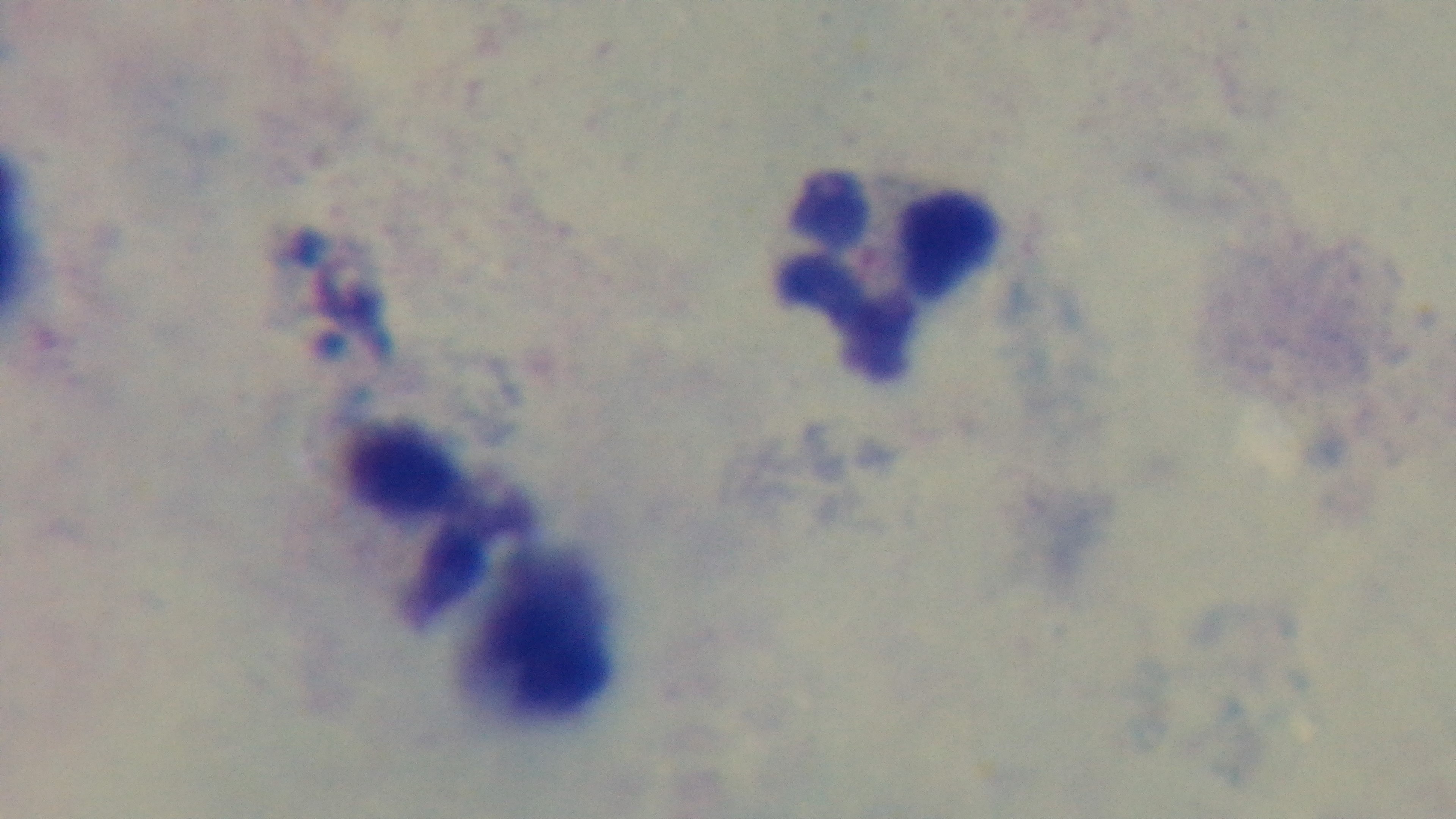
{
  "objective": "100x oil immersion",
  "modality": "light microscopy",
  "stain": "Giemsa",
  "field_of_view": "single",
  "malaria_status": "negative",
  "capture": "mounted 4K digital camera",
  "preparation": "thick"
}